Assess the morphology of the erythrocytes.
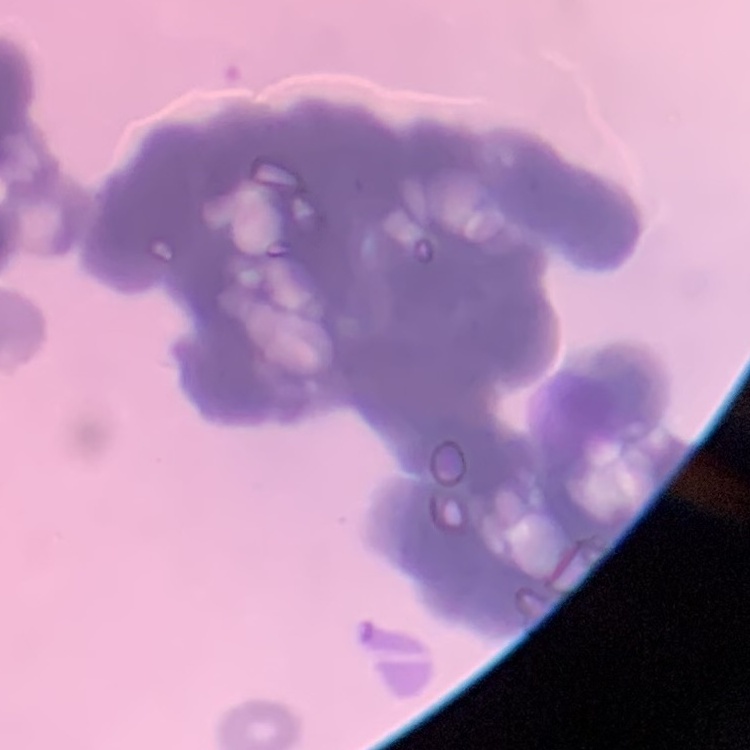

Rouleaux formation.

Field's or Giemsa stain. Square crop of a larger photomicrograph. Thin peripheral smear.